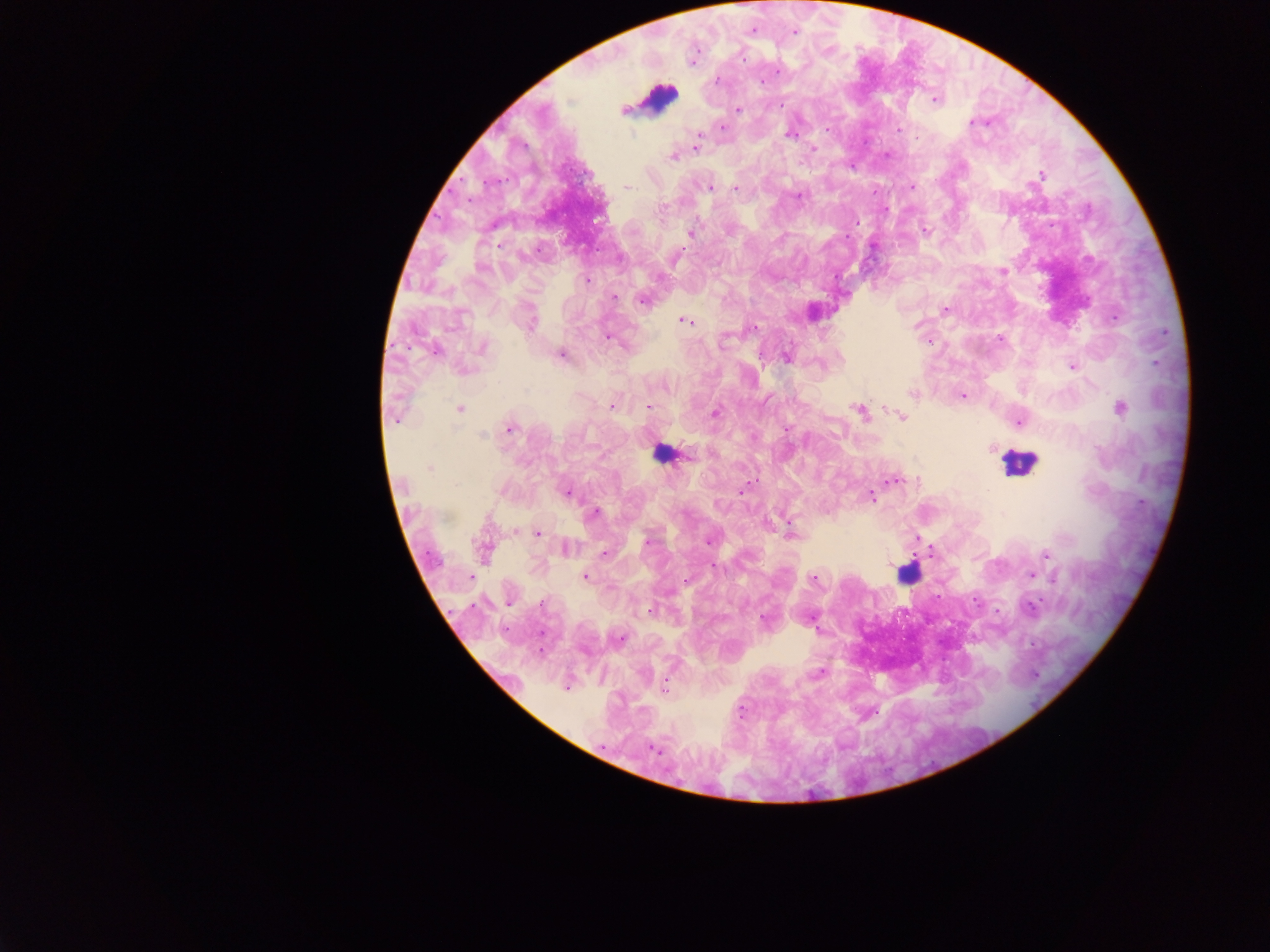

Approximate centers as [x, y] in pixels. Plasmodium parasite locations: [751, 31], [795, 31], [693, 57], [717, 79], [761, 81], [935, 99], [780, 106], [737, 110], [976, 122], [722, 127], [828, 130], [898, 130], [790, 134], [918, 138], [697, 147], [812, 148], [887, 153], [674, 156], [1041, 174], [625, 186], [709, 186], [910, 186], [735, 188], [884, 210], [924, 230], [689, 233], [873, 245], [674, 258], [1003, 272], [587, 280], [613, 297], [643, 299], [945, 310], [528, 320], [684, 320], [916, 325], [753, 327], [607, 336], [1000, 339], [929, 340], [482, 347], [435, 350], [561, 353], [786, 357], [1072, 366], [463, 369], [913, 392], [961, 395], [612, 405], [648, 407], [459, 408], [1120, 408], [859, 411], [396, 413], [715, 413], [902, 416], [1019, 421], [508, 429], [990, 447], [431, 467], [891, 479], [742, 491], [567, 492], [871, 496], [594, 512], [538, 533], [790, 535], [917, 537], [709, 540], [648, 542], [566, 547], [931, 550], [484, 551], [604, 553], [1046, 555], [1030, 575], [584, 576], [813, 578], [685, 581], [509, 602], [764, 619], [617, 638], [818, 673], [566, 684], [663, 686], [652, 748]. Leukocyte locations: [659, 98], [662, 453], [1019, 464], [906, 573]. Mobile-phone photograph taken through the microscope. Thick blood film. Image is 1270×952 pixels. Collected in Ghana. One field of view.